Report the malaria status of this cell.
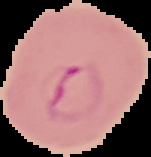
It is parasitized.

Image is 151×157 pixels. The area outside the segmented cell region is set to black. From a thin blood smear.